Outline platelets.
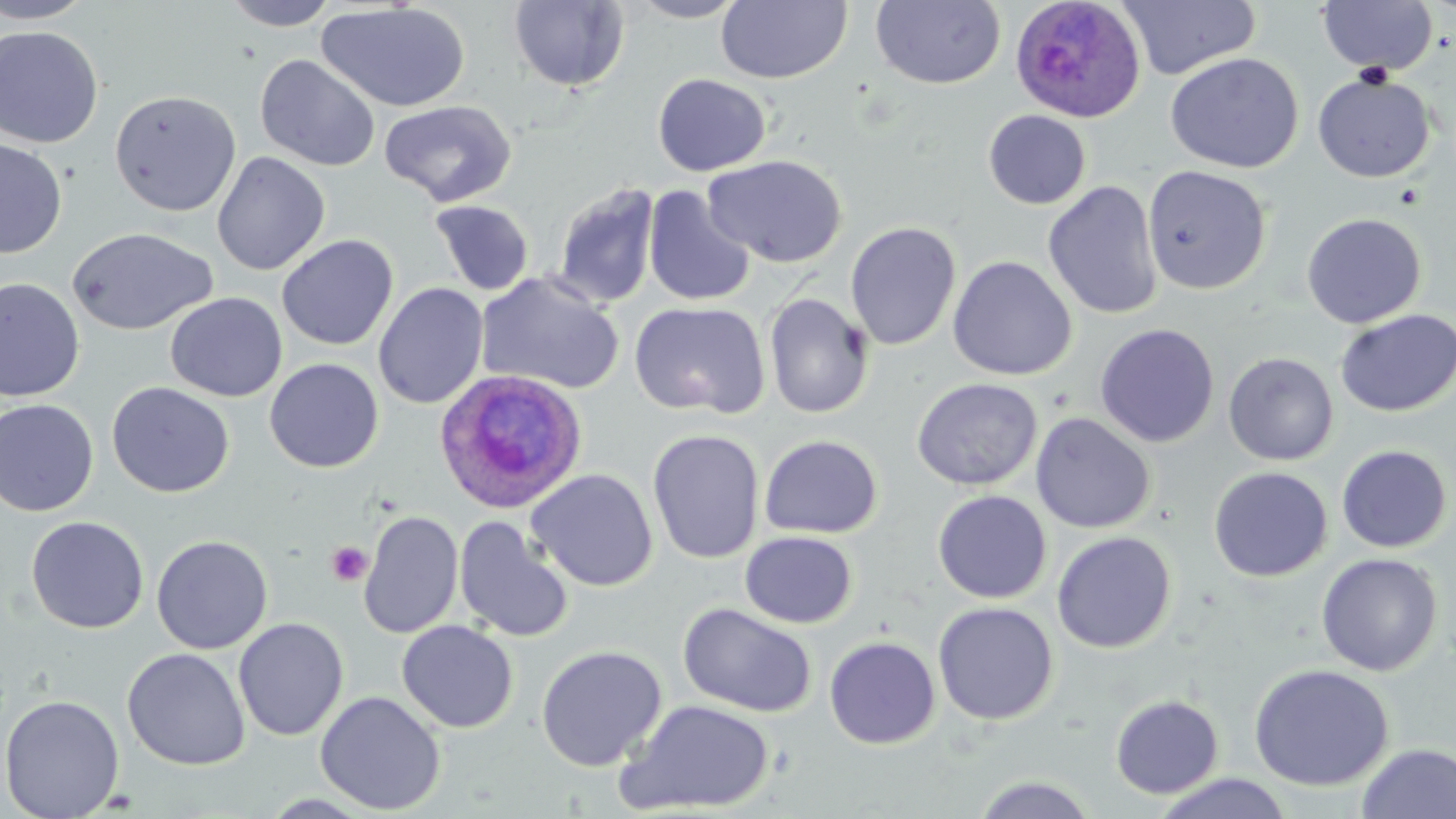

Approximate bounding boxes as (x1, y1, x2, y2) in pixels.
Platelets: (326, 541, 373, 586).

Summary:
  - Uninfected red blood cell locations: (0, 0, 97, 23), (222, 0, 340, 30), (626, 0, 751, 22), (716, 0, 852, 85), (871, 0, 1006, 89), (509, 1, 630, 92), (1119, 1, 1262, 80), (1317, 1, 1438, 77), (316, 3, 471, 113), (0, 25, 103, 149), (1165, 52, 1304, 173), (255, 54, 380, 172), (1312, 71, 1435, 183), (653, 73, 771, 176), (109, 89, 242, 217), (379, 99, 517, 207), (983, 110, 1091, 209), (0, 138, 67, 258), (211, 151, 330, 275), (703, 154, 848, 268), (1142, 165, 1272, 295), (1043, 180, 1163, 321), (552, 183, 661, 309), (643, 185, 756, 307), (429, 197, 660, 303), (430, 200, 534, 296), (1301, 212, 1427, 329), (844, 221, 962, 350), (66, 226, 218, 336), (276, 234, 398, 351), (948, 256, 1077, 381), (475, 271, 625, 396), (0, 278, 85, 402), (373, 282, 489, 409), (164, 292, 287, 402), (763, 292, 874, 418), (629, 300, 770, 419), (1335, 309, 1456, 417), (1095, 323, 1220, 447), (1224, 352, 1338, 466), (264, 358, 384, 473), (911, 378, 1043, 491), (106, 381, 235, 498), (0, 399, 99, 517), (1030, 412, 1156, 534), (647, 429, 764, 564), (759, 434, 883, 539), (1336, 444, 1453, 553), (1208, 467, 1333, 582), (526, 468, 658, 591), (932, 491, 1052, 604), (357, 510, 464, 639), (26, 515, 149, 633), (454, 517, 573, 644), (740, 530, 858, 628), (1051, 531, 1176, 654), (152, 534, 273, 654), (1316, 553, 1443, 677), (677, 602, 817, 718), (933, 602, 1058, 725), (233, 617, 349, 741), (397, 620, 519, 733), (824, 635, 941, 749), (536, 644, 667, 772), (122, 648, 250, 770), (1248, 663, 1394, 791), (314, 690, 446, 815), (0, 694, 124, 818), (1110, 694, 1224, 799), (616, 699, 776, 814), (1357, 743, 1456, 819), (1149, 771, 1295, 818), (971, 774, 1100, 819), (258, 793, 379, 817)
  - Plasmodium ovale-infected red blood cell locations: (1009, 0, 1145, 122), (434, 368, 589, 514)
  - Slide-level diagnosis: Plasmodium ovale
  - Image size: 1456×819 pixels
  - Modality: optical microscopy
  - Preparation: thin blood smear
  - Field of view: one of a larger specimen
  - Stain: May-Grünwald-Giemsa
  - Magnification: 1000x